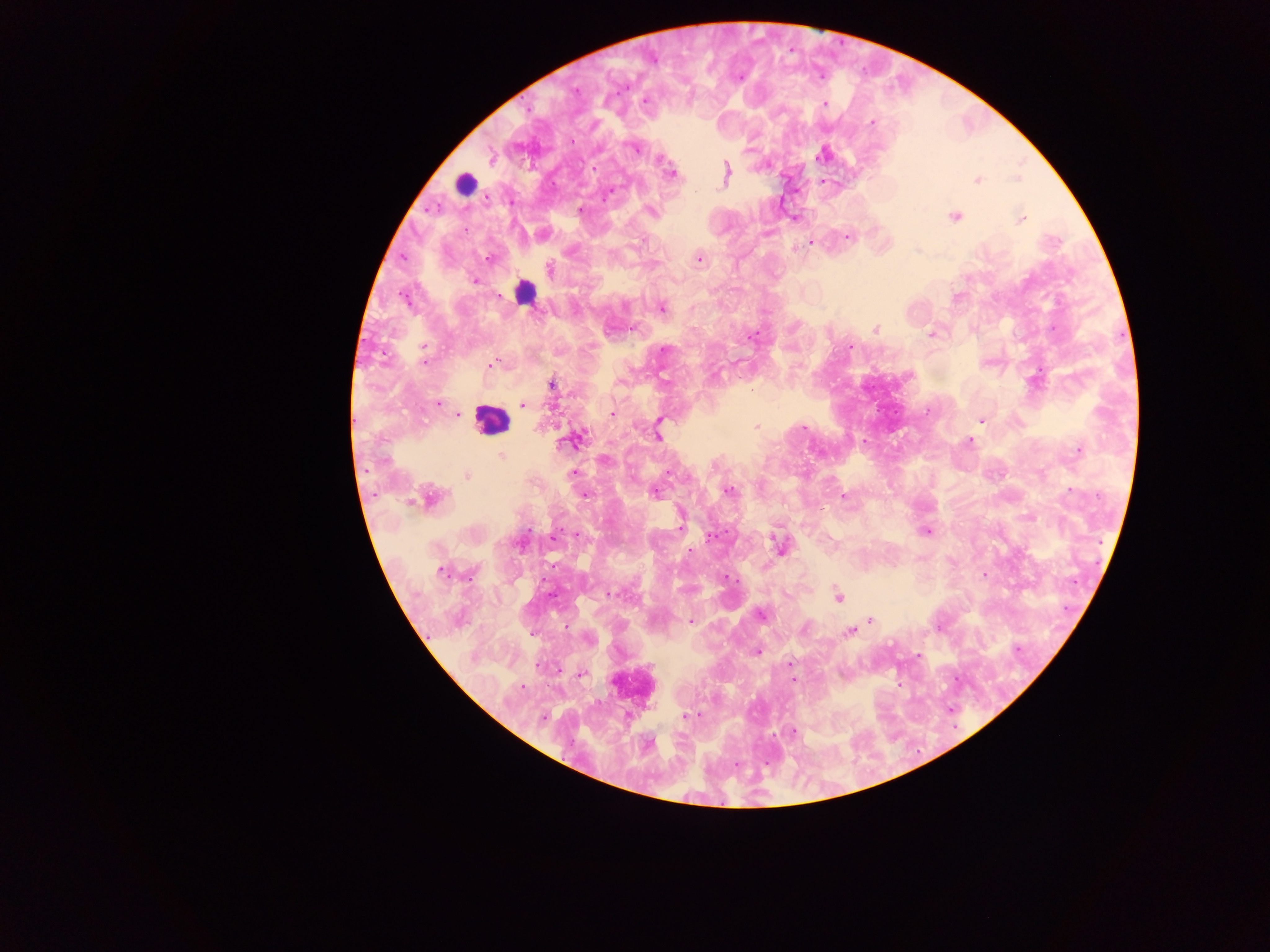

capture = mobile-phone photograph through a microscope
leukocyte locations = approximate centers as {x, y} in pixels: {465, 184}, {526, 288}, {490, 420}, {633, 684}
field of view = single
image size = 1270×952 pixels
preparation = thick blood smear
country = Ghana
malaria parasite locations = approximate centers as {x, y} in pixels: {651, 59}, {737, 77}, {575, 92}, {645, 101}, {825, 104}, {872, 123}, {571, 139}, {635, 148}, {490, 154}, {822, 154}, {592, 169}, {671, 173}, {725, 174}, {1017, 178}, {978, 179}, {822, 181}, {607, 194}, {581, 210}, {651, 211}, {953, 216}, {795, 217}, {1021, 219}, {767, 232}, {542, 233}, {848, 236}, {811, 241}, {918, 249}, {490, 258}, {699, 258}, {559, 274}, {475, 279}, {957, 298}, {662, 308}, {633, 328}, {876, 329}, {932, 334}, {753, 335}, {850, 346}, {492, 364}, {551, 384}, {439, 403}, {523, 405}, {456, 414}, {612, 414}, {982, 421}, {756, 427}, {658, 433}, {572, 440}, {969, 441}, {1079, 450}, {501, 455}, {603, 460}, {669, 472}, {573, 473}, {466, 475}, {727, 490}, {653, 491}, {584, 494}, {844, 495}, {428, 498}, {926, 530}, {711, 535}, {521, 542}, {780, 546}, {688, 552}, {440, 570}, {983, 575}, {725, 577}, {608, 593}, {785, 593}, {839, 596}, {760, 614}, {870, 620}, {690, 621}, {939, 627}, {850, 632}, {533, 634}, {588, 638}, {757, 651}, {917, 655}, {790, 662}, {581, 674}, {792, 679}, {900, 684}, {684, 716}, {542, 718}, {791, 733}, {649, 743}